Outline platelets.
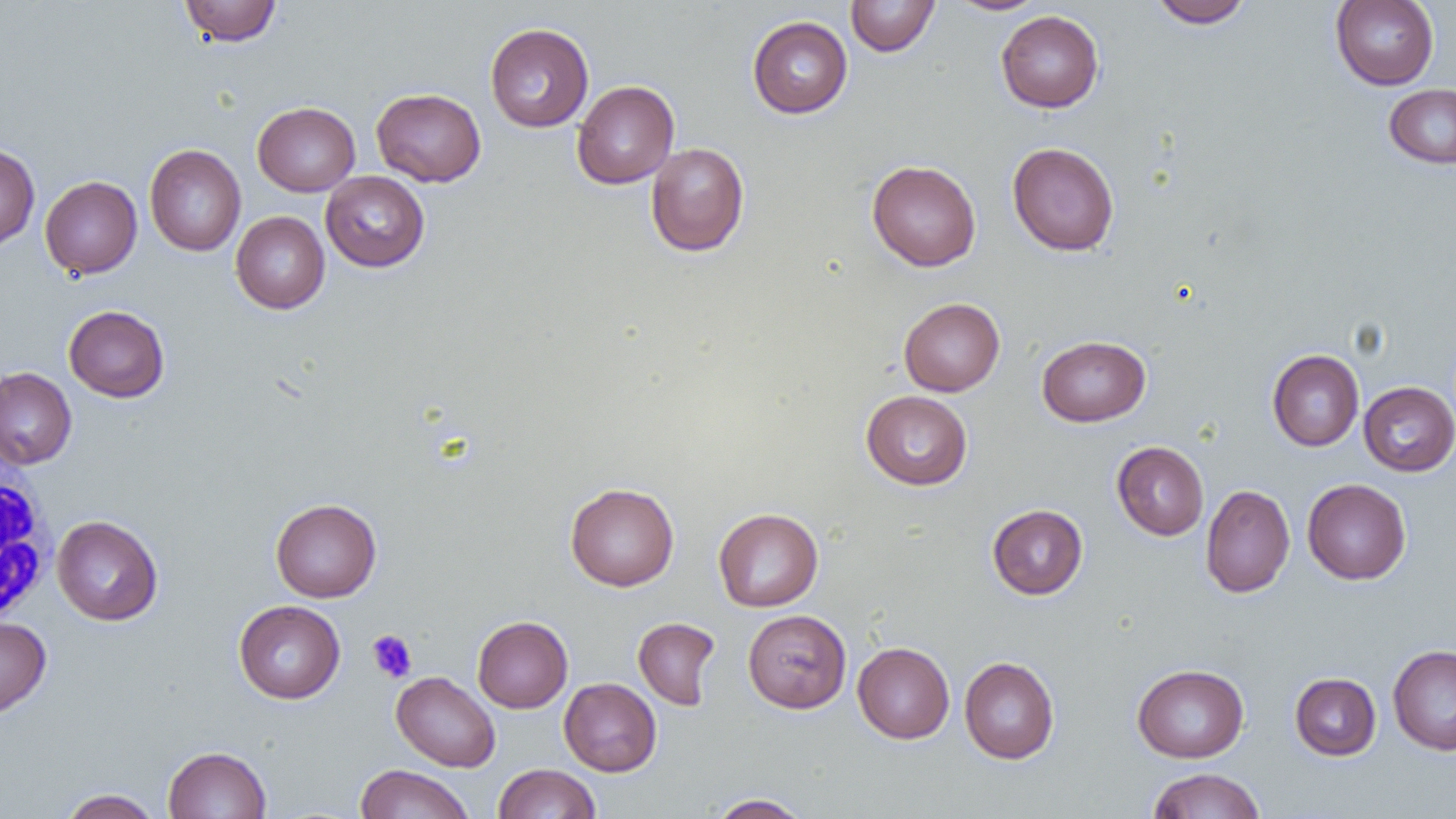

Approximate bounding boxes as (x1,y1)-(x2,y2) corner pairs in pixels.
Platelets: (367,630)-(417,682).

Uninfected red blood cell locations: (179,0)-(281,46), (845,0)-(940,57), (947,0)-(1048,15), (1148,0)-(1253,28), (1330,0)-(1439,90), (996,10)-(1104,112), (747,16)-(853,118), (485,22)-(594,132), (572,80)-(679,189), (1384,84)-(1456,169), (371,88)-(486,187), (252,102)-(360,196), (646,142)-(749,257), (1007,142)-(1120,256), (0,143)-(40,252), (144,144)-(246,256), (866,160)-(981,271), (320,171)-(430,272), (40,175)-(142,279), (230,211)-(330,314), (898,297)-(1005,396), (64,305)-(169,402), (1037,335)-(1150,427), (1267,349)-(1364,451), (0,367)-(77,469), (1358,381)-(1456,476), (860,390)-(973,490), (1112,441)-(1209,540), (1302,478)-(1411,585), (565,482)-(679,591), (1200,484)-(1295,597), (270,497)-(381,602), (987,504)-(1088,599), (713,507)-(823,612), (51,515)-(163,625), (233,600)-(345,703), (743,609)-(851,713), (472,615)-(573,713), (0,616)-(51,718), (633,617)-(720,709), (853,642)-(954,743), (1388,645)-(1456,755), (959,656)-(1060,764), (1132,664)-(1249,762), (391,672)-(501,771), (1290,672)-(1381,760), (559,678)-(662,776), (163,746)-(272,818), (493,763)-(600,818), (354,764)-(475,819), (1146,768)-(1266,819), (58,788)-(162,818), (706,793)-(812,818). White blood cell locations: (0,455)-(56,633). Slide-level diagnosis: no evidence of blood parasites. Captured at 1000x magnification. One field of a larger specimen. Thin blood smear. Image is 1456×819 pixels. Light microscopy.